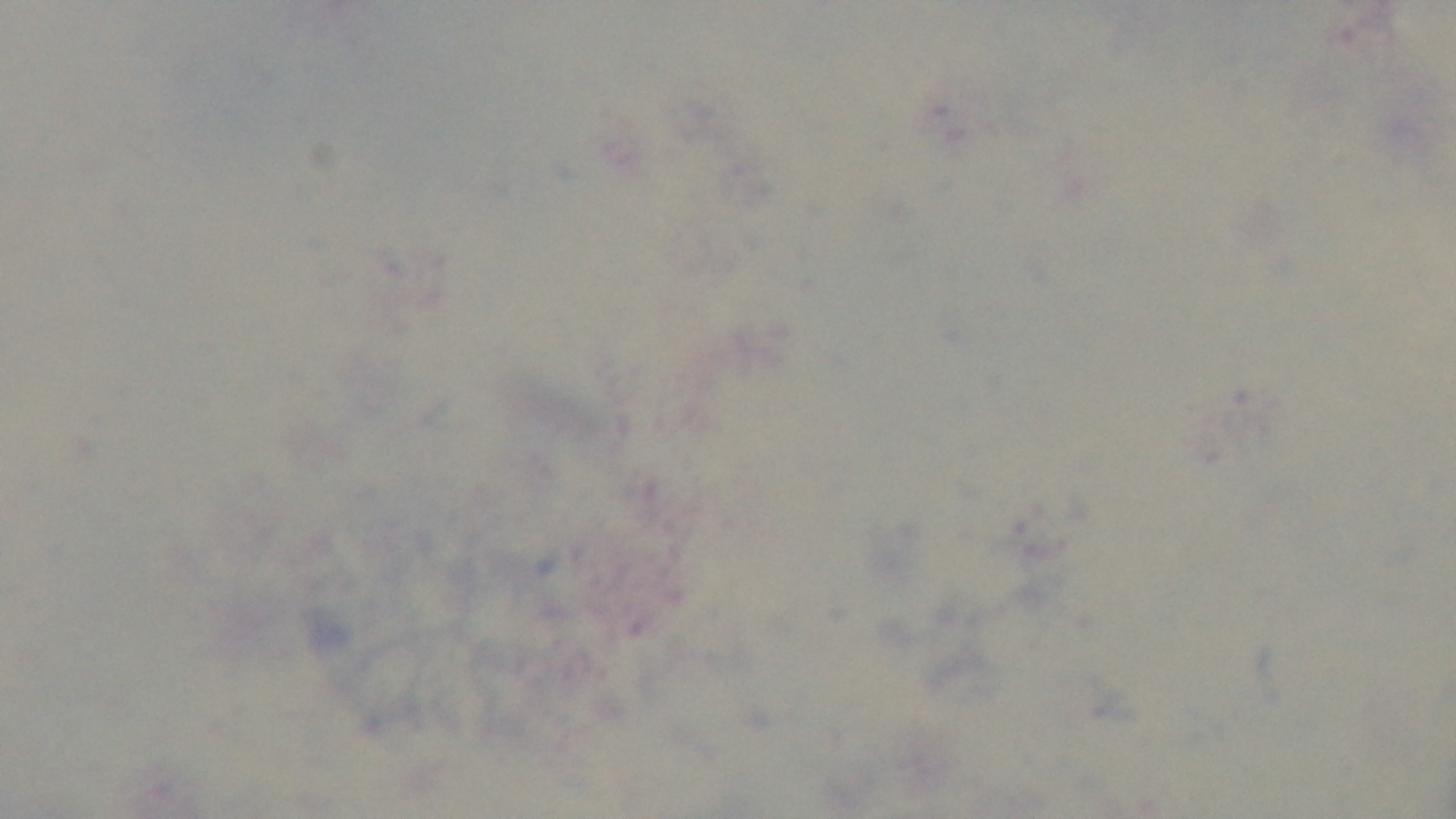
modality = light microscopy
capture = mounted 4K digital camera
field of view = single
stain = Giemsa
objective = 100x oil immersion
malaria status = negative
preparation = thick blood film